Point out each Plasmodium parasite.
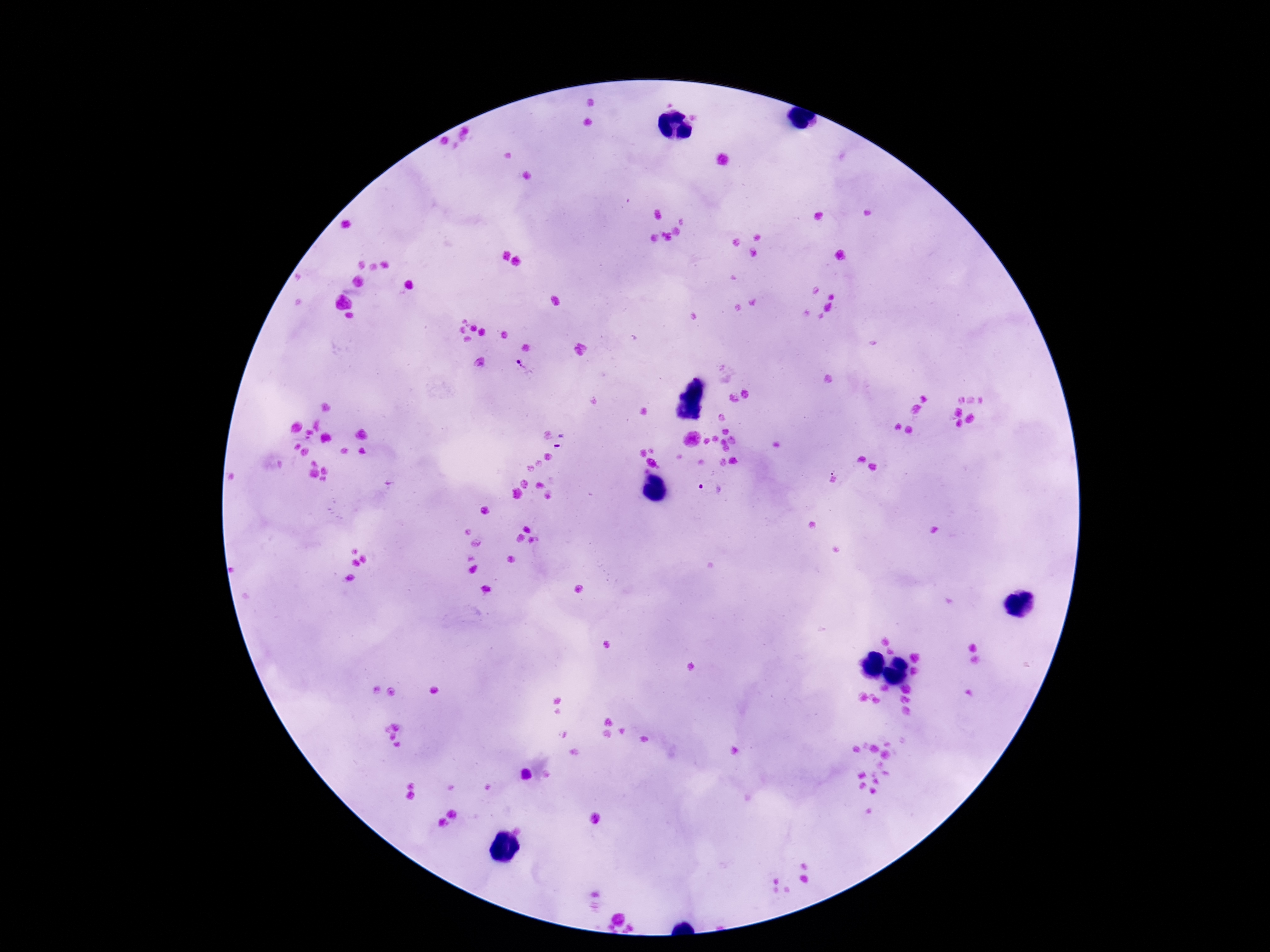
Approximate centers as (x, y) in pixels.
Plasmodium parasites: (524, 368), (561, 442), (711, 488).

Single field of view. 100x magnification. Thick blood film. Patient malaria status: positive. Image is 1270×952 pixels. Smartphone photograph taken through the microscope eyepiece. Giemsa-stained preparation.